State which parasite is depicted.
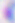
Toxoplasma gondii.

400x magnification. Micrograph.